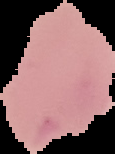
Summary:
  - Result: no malaria parasites detected
  - Preparation: thin blood film
  - Image type: segmented cell region on a black background
  - Image size: 115×154 pixels